Report the malaria status of this cell.
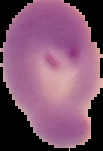

Parasitized.

Image is 103×151 pixels. Segmented cell region on a black background. From a thin blood film.